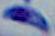
modality = photomicrograph
identification = Toxoplasma gondii
magnification = 1000x